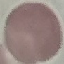

Summary:
  - Result: negative for malaria parasites
  - Image type: cell patch, automatically extracted from a larger field of view and resized to 64 × 64 pixels
  - Capture: smartphone camera at the microscope eyepiece
  - Preparation: thin smear
  - Stain: Giemsa